Identify the parasite.
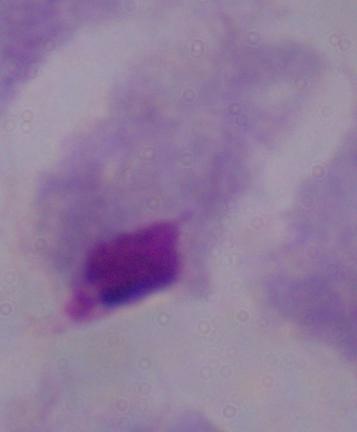
A trichomonad.

magnification = 1000x
modality = photomicrograph